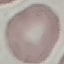

Malaria status: uninfected. Giemsa-stained preparation. Cell patch, automatically extracted from a larger field of view and resized to 64 × 64 pixels. Acquired by smartphone through the microscope eyepiece. Thin blood film.